Assess this cell for malaria.
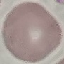

It is uninfected.

Cell patch, automatically extracted from a larger field of view and resized to 64 × 64 pixels. Giemsa-stained preparation. Thin blood film. Acquired by smartphone through the microscope eyepiece.